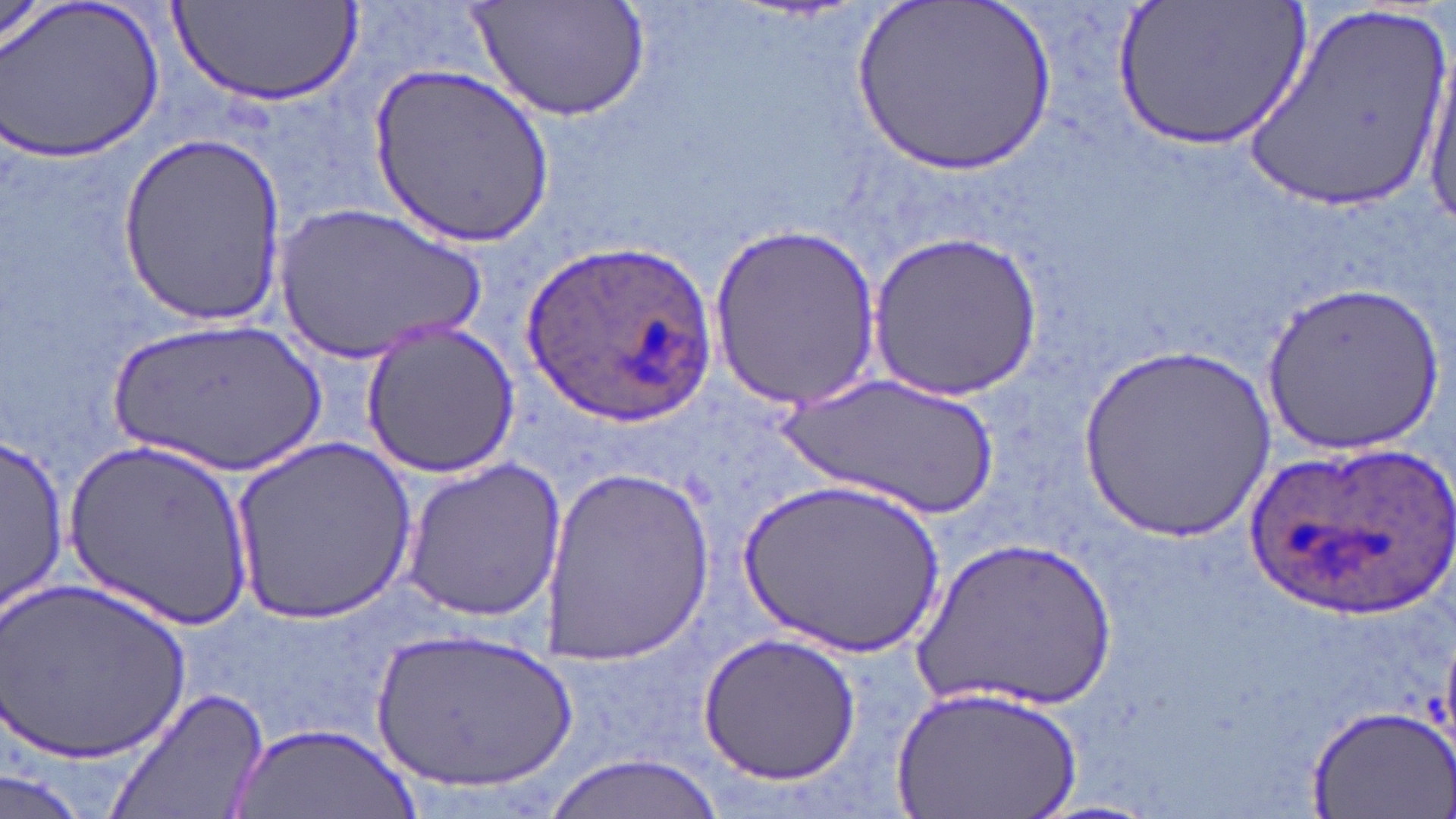

Approximate bounding boxes as named x1/y1/x2/y2 corners in pixels. Plasmodium ovale-infected red blood cell locations: (x1=519, y1=239, x2=717, y2=426), (x1=1238, y1=434, x2=1450, y2=620). Uninfected red blood cell locations: (x1=2, y1=0, x2=166, y2=163), (x1=468, y1=0, x2=653, y2=122), (x1=850, y1=0, x2=1060, y2=180), (x1=1117, y1=0, x2=1311, y2=153), (x1=1245, y1=3, x2=1452, y2=218), (x1=170, y1=5, x2=357, y2=107), (x1=1423, y1=46, x2=1455, y2=240), (x1=372, y1=62, x2=554, y2=246), (x1=117, y1=133, x2=287, y2=327), (x1=274, y1=199, x2=489, y2=365), (x1=706, y1=222, x2=883, y2=412), (x1=865, y1=230, x2=1043, y2=402), (x1=1263, y1=278, x2=1443, y2=452), (x1=107, y1=318, x2=327, y2=479), (x1=361, y1=318, x2=520, y2=479), (x1=1077, y1=339, x2=1279, y2=540), (x1=773, y1=368, x2=1008, y2=525), (x1=3, y1=434, x2=69, y2=615), (x1=65, y1=436, x2=254, y2=631), (x1=230, y1=437, x2=417, y2=625), (x1=401, y1=459, x2=568, y2=622), (x1=539, y1=463, x2=713, y2=664), (x1=731, y1=474, x2=948, y2=660), (x1=908, y1=532, x2=1120, y2=718), (x1=5, y1=580, x2=192, y2=768), (x1=371, y1=626, x2=577, y2=798), (x1=699, y1=632, x2=862, y2=785), (x1=888, y1=682, x2=1082, y2=819), (x1=103, y1=685, x2=272, y2=819), (x1=1302, y1=703, x2=1456, y2=819), (x1=230, y1=723, x2=414, y2=818), (x1=542, y1=753, x2=722, y2=819), (x1=0, y1=769, x2=86, y2=819). Slide-level diagnosis: Plasmodium ovale. Light microscopy. One field of a larger specimen. May-Grünwald-Giemsa-stained preparation. Thin blood smear. Image is 1456×819 pixels. Captured at 1000x magnification.